State which parasite is depicted.
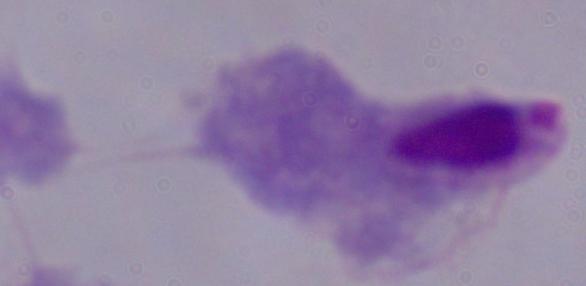
A trichomonad.

{
  "modality": "photomicrograph",
  "magnification": "1000x"
}